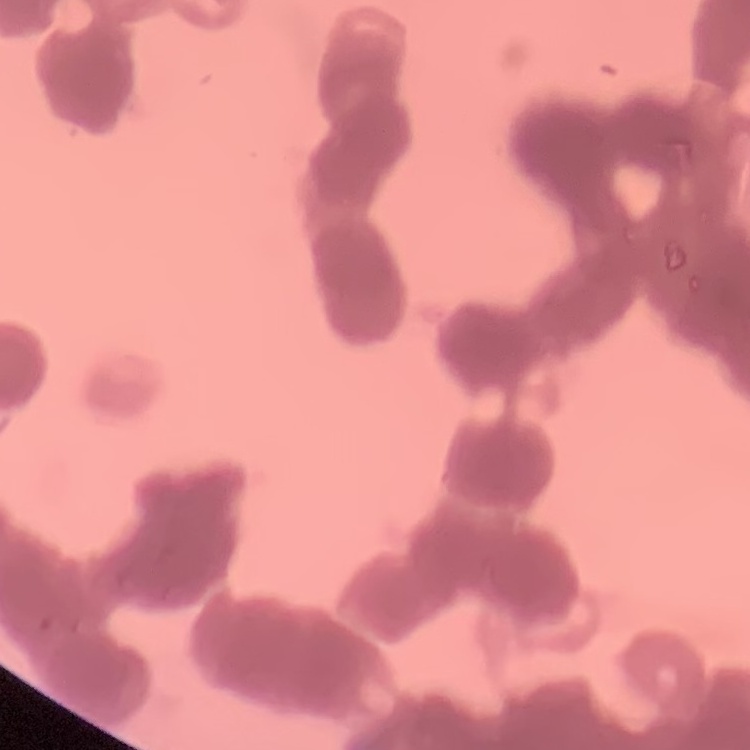
{
  "erythrocyte_morphology": "rouleaux formation",
  "preparation": "thin peripheral smear",
  "image_type": "square crop of a larger photomicrograph",
  "stain": "Field's or Giemsa"
}